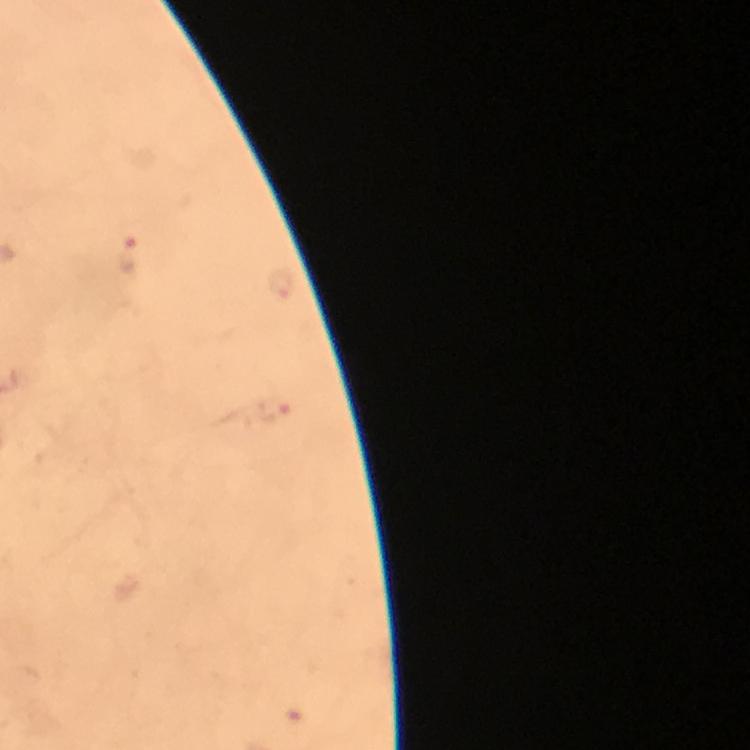 Approximate centers as (x, y) in pixels. Plasmodium parasite locations: (130, 254), (276, 409). Thick blood film. Immersion oil was used. At 100x magnification. From a malaria diagnostic workup. Photographed through the microscope with a smartphone camera. Image is 750×750 pixels. A crop from one field of view. Giemsa stain.